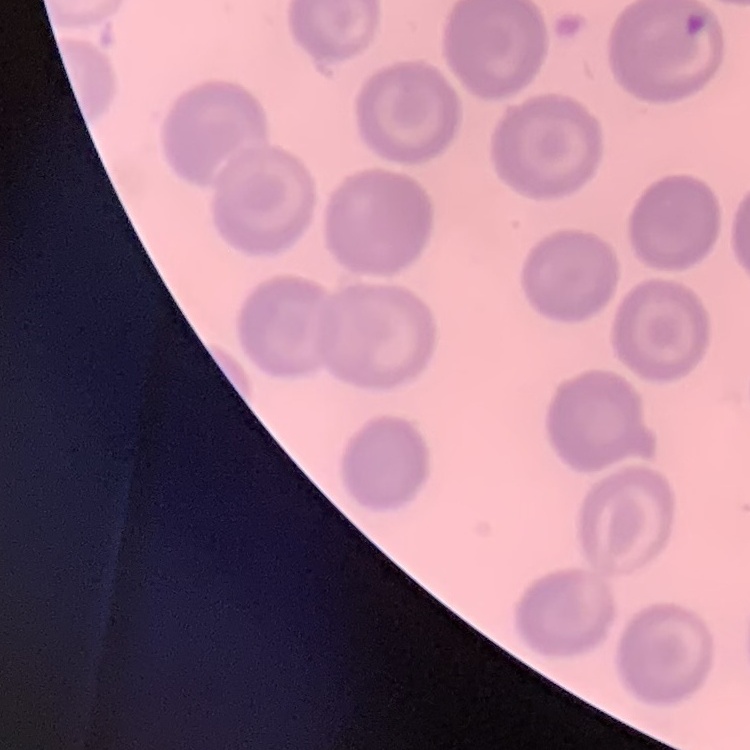

erythrocyte_morphology: no rouleaux formation
image_type: one tile cut from a larger photomicrograph
preparation: thin blood smear
stain: Field's or Giemsa